Classify this cell by malaria status.
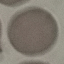
Uninfected.

Giemsa stain. Cell patch, automatically extracted from a larger field of view and resized to 64 × 64 pixels. Photographed with a smartphone camera at the microscope eyepiece. Thin blood smear.